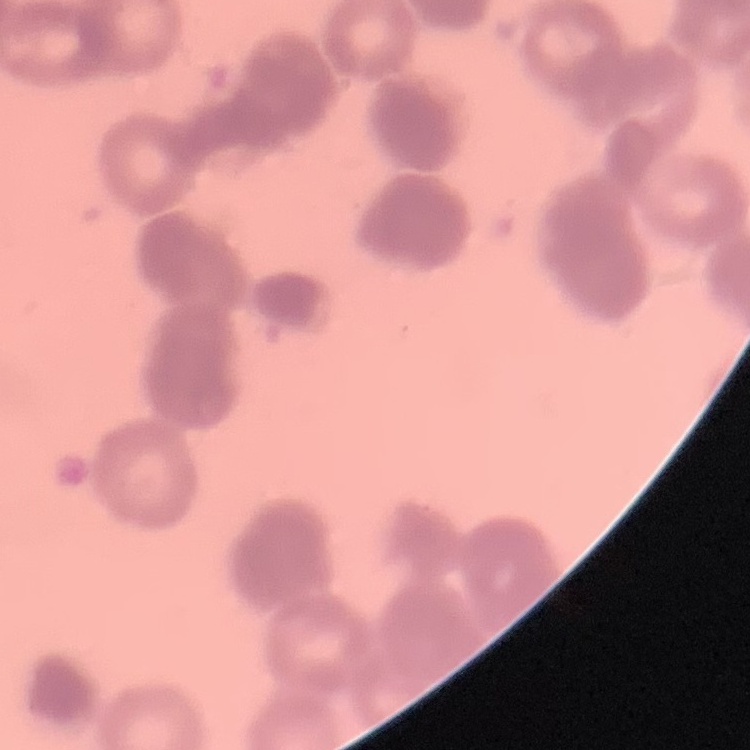 The erythrocytes show rouleaux formation. One tile cut from a larger photomicrograph. Thin blood film. Field's or Giemsa stain.